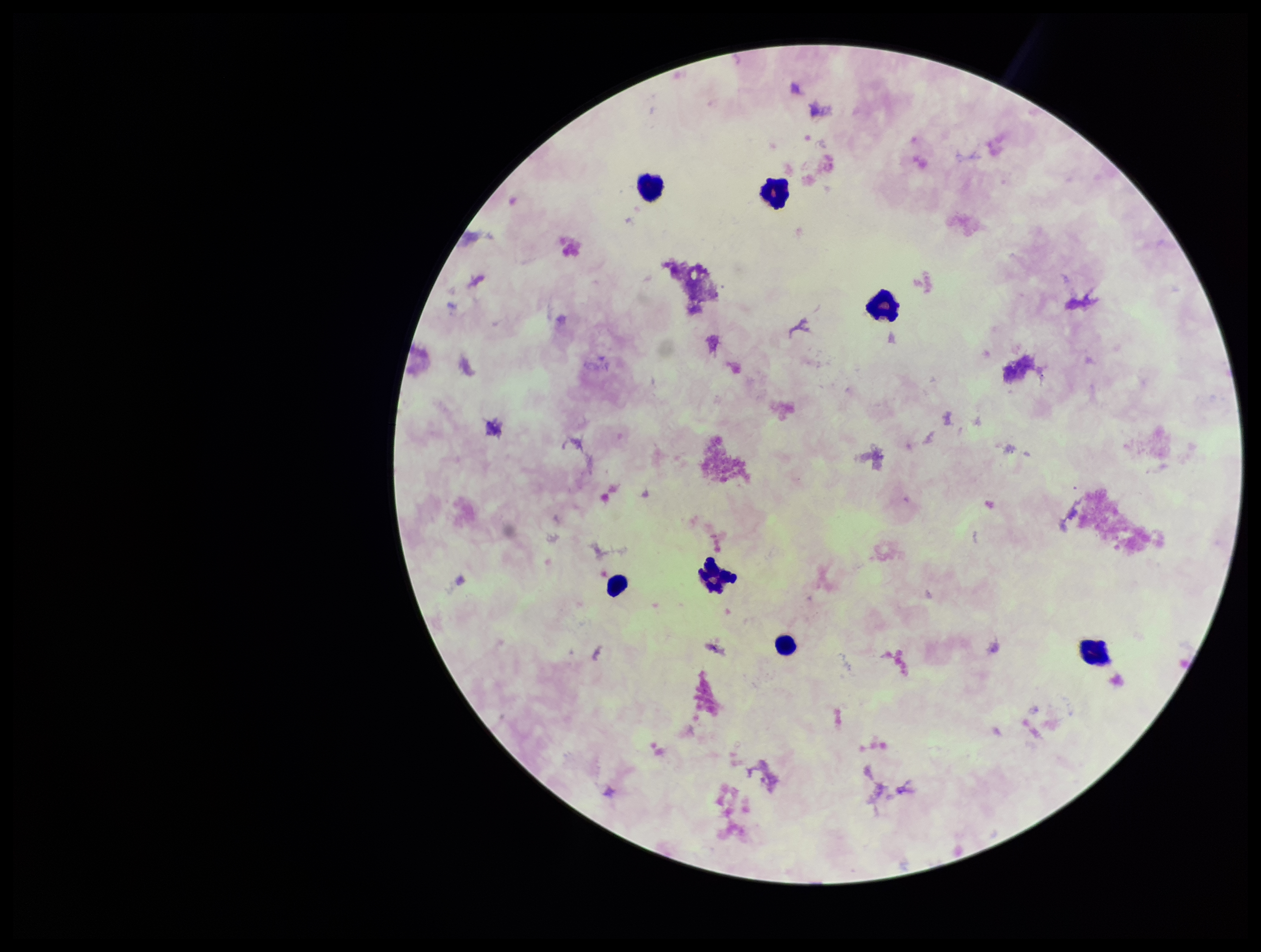
Patient malaria status: negative. Preparation: thick. Plasmodium parasites: none seen. Leukocyte count: 7. One field from this slide. Parasite count: 0. Stained with Giemsa. Photographed through the microscope eyepiece with a smartphone camera. Image is 1261×952 pixels.